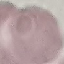

Malaria status: uninfected. Giemsa stain. Automatically extracted cell patch, resized to 64 × 64 pixels. Thin blood smear. Photographed with a smartphone camera at the microscope eyepiece.